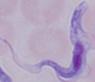
Micrograph. A trypanosome is shown. Captured at 1000x magnification.